Report the malaria status of this cell.
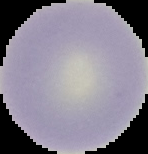

It is uninfected.

Summary:
  - Image size: 148×154 pixels
  - Image type: cell region segmented out of the field of view; surrounding area masked to black
  - Preparation: thin blood film